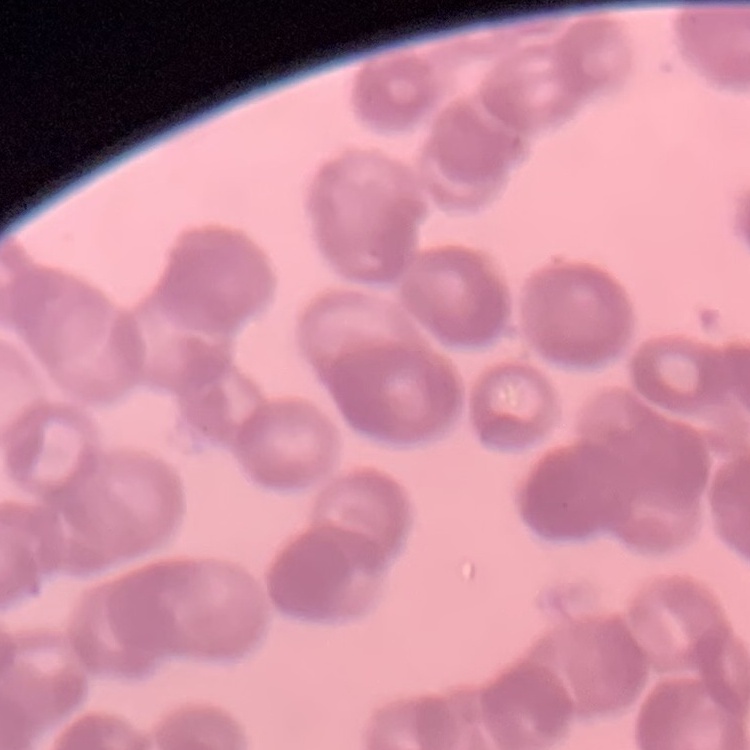 The red blood cells exhibit rouleaux formation. Stained with either Field's or Giemsa. Square crop of a larger photomicrograph. Thin blood smear.